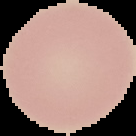
Summary:
  - Image type: cell region segmented out of the field of view; surrounding area masked to black
  - Image size: 136×136 pixels
  - Result: no Plasmodium parasites detected
  - Preparation: thin blood smear